Assess this cell for malaria.
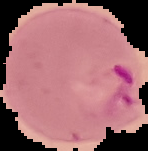

Parasitized.

preparation = thin blood film
image size = 148×151 pixels
image type = cell region segmented out of the field of view; surrounding area masked to black